Name the cell type shown.
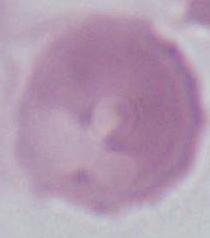

This is an erythrocyte.

Summary:
  - Magnification: 1000x
  - Modality: micrograph